Report the malaria status of this cell.
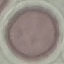
It is uninfected.

Automatically extracted cell patch, resized to 64 × 64 pixels. Thin blood smear. Giemsa-stained preparation. Acquired by smartphone through the microscope eyepiece.